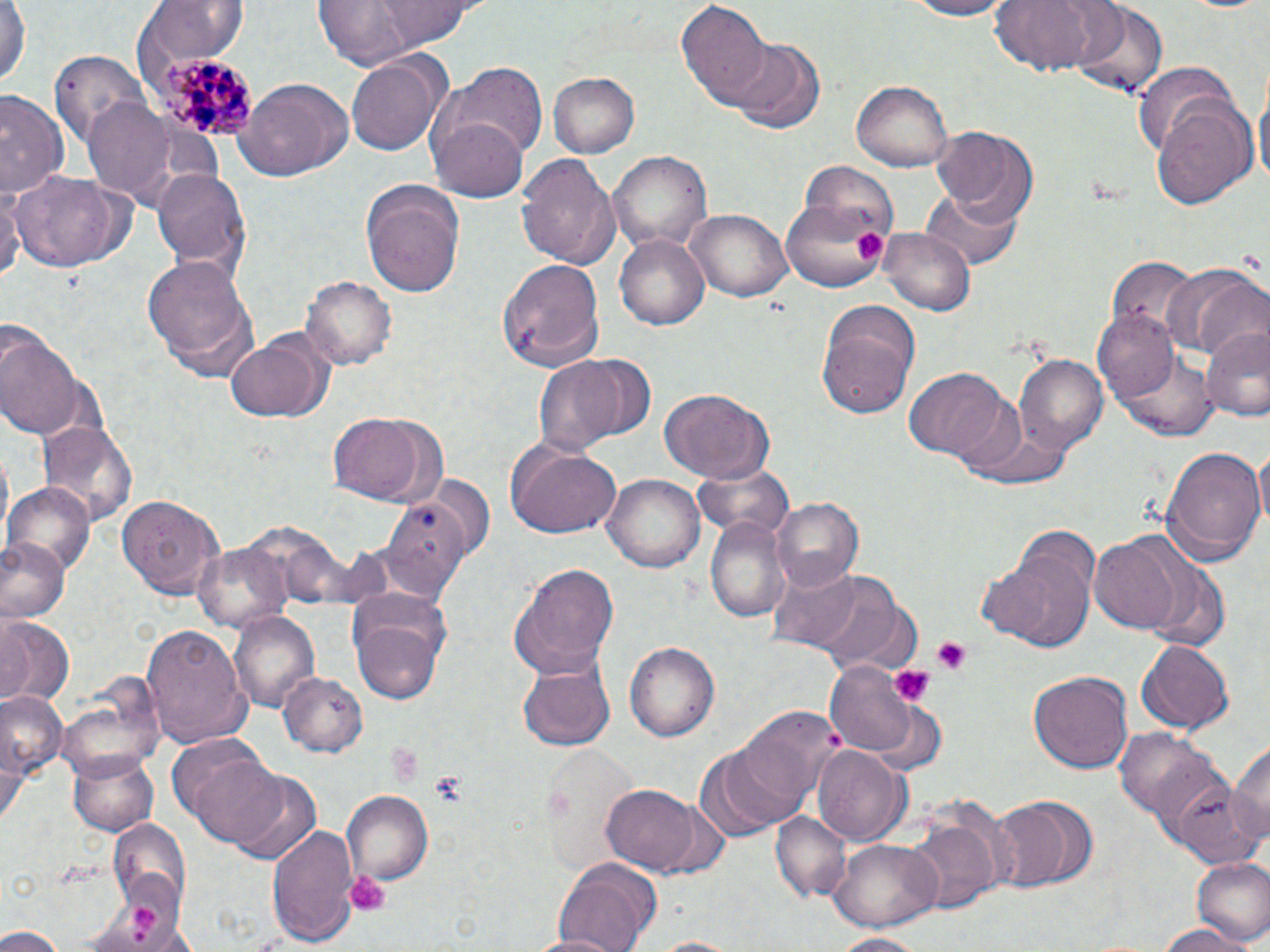

Summary:
  - Coordinate format: approximate bounding boxes as named x1/y1/x2/y2 corners in pixels
  - Uninfected red blood cell locations: (x1=1, y1=0, x2=30, y2=92), (x1=375, y1=0, x2=480, y2=47), (x1=898, y1=0, x2=1021, y2=20), (x1=994, y1=0, x2=1108, y2=77), (x1=142, y1=2, x2=248, y2=72), (x1=310, y1=2, x2=457, y2=67), (x1=677, y1=2, x2=770, y2=109), (x1=1070, y1=2, x2=1169, y2=101), (x1=728, y1=36, x2=829, y2=135), (x1=345, y1=50, x2=448, y2=157), (x1=49, y1=51, x2=153, y2=157), (x1=1133, y1=64, x2=1236, y2=154), (x1=451, y1=65, x2=549, y2=158), (x1=549, y1=73, x2=641, y2=158), (x1=236, y1=79, x2=353, y2=184), (x1=429, y1=81, x2=537, y2=203), (x1=852, y1=81, x2=953, y2=172), (x1=1255, y1=81, x2=1270, y2=193), (x1=0, y1=92, x2=64, y2=202), (x1=1147, y1=95, x2=1256, y2=208), (x1=83, y1=99, x2=178, y2=205), (x1=931, y1=125, x2=1039, y2=226), (x1=608, y1=152, x2=712, y2=255), (x1=516, y1=153, x2=620, y2=270), (x1=149, y1=166, x2=251, y2=276), (x1=9, y1=169, x2=134, y2=274), (x1=0, y1=176, x2=21, y2=289), (x1=359, y1=177, x2=466, y2=297), (x1=923, y1=185, x2=1022, y2=271), (x1=782, y1=188, x2=892, y2=294), (x1=682, y1=209, x2=793, y2=304), (x1=881, y1=228, x2=973, y2=315), (x1=613, y1=232, x2=710, y2=332), (x1=142, y1=249, x2=262, y2=380), (x1=1105, y1=257, x2=1197, y2=340), (x1=499, y1=258, x2=606, y2=370), (x1=1164, y1=265, x2=1263, y2=357), (x1=302, y1=274, x2=398, y2=372), (x1=814, y1=296, x2=922, y2=417), (x1=1093, y1=310, x2=1183, y2=406), (x1=1200, y1=324, x2=1270, y2=422), (x1=226, y1=328, x2=333, y2=423), (x1=0, y1=330, x2=84, y2=443), (x1=1116, y1=347, x2=1216, y2=440), (x1=564, y1=352, x2=657, y2=442), (x1=1013, y1=354, x2=1108, y2=454), (x1=531, y1=356, x2=628, y2=457), (x1=906, y1=369, x2=1012, y2=461), (x1=659, y1=389, x2=773, y2=482), (x1=964, y1=413, x2=1079, y2=489), (x1=327, y1=414, x2=434, y2=504), (x1=36, y1=418, x2=138, y2=526), (x1=505, y1=442, x2=621, y2=538), (x1=1254, y1=444, x2=1270, y2=536), (x1=1163, y1=445, x2=1266, y2=564), (x1=692, y1=461, x2=796, y2=541), (x1=606, y1=471, x2=705, y2=571), (x1=428, y1=473, x2=493, y2=555), (x1=6, y1=485, x2=94, y2=578), (x1=118, y1=494, x2=226, y2=597), (x1=374, y1=497, x2=470, y2=605), (x1=768, y1=498, x2=864, y2=589), (x1=705, y1=515, x2=791, y2=625), (x1=0, y1=537, x2=68, y2=625), (x1=1089, y1=537, x2=1183, y2=634), (x1=194, y1=542, x2=293, y2=631), (x1=984, y1=542, x2=1099, y2=655), (x1=1141, y1=560, x2=1230, y2=652), (x1=509, y1=564, x2=621, y2=680), (x1=767, y1=565, x2=864, y2=651), (x1=804, y1=572, x2=922, y2=676), (x1=348, y1=593, x2=452, y2=703), (x1=2, y1=614, x2=74, y2=702), (x1=230, y1=614, x2=320, y2=714), (x1=139, y1=619, x2=252, y2=747), (x1=1135, y1=638, x2=1234, y2=735), (x1=624, y1=640, x2=720, y2=741), (x1=519, y1=661, x2=613, y2=751), (x1=822, y1=662, x2=937, y2=762), (x1=1027, y1=670, x2=1133, y2=775), (x1=278, y1=672, x2=365, y2=757), (x1=59, y1=678, x2=165, y2=777), (x1=1, y1=688, x2=65, y2=790), (x1=738, y1=706, x2=842, y2=810), (x1=1115, y1=727, x2=1227, y2=828), (x1=1229, y1=732, x2=1270, y2=847), (x1=697, y1=741, x2=809, y2=840), (x1=545, y1=748, x2=640, y2=873), (x1=812, y1=748, x2=911, y2=845), (x1=70, y1=750, x2=158, y2=836), (x1=187, y1=752, x2=291, y2=845), (x1=228, y1=771, x2=323, y2=867), (x1=601, y1=783, x2=709, y2=876), (x1=1174, y1=785, x2=1264, y2=868), (x1=341, y1=790, x2=433, y2=887), (x1=987, y1=794, x2=1098, y2=894), (x1=773, y1=813, x2=850, y2=901), (x1=907, y1=816, x2=1003, y2=912), (x1=110, y1=817, x2=190, y2=911), (x1=267, y1=822, x2=360, y2=951), (x1=827, y1=837, x2=942, y2=933), (x1=1191, y1=856, x2=1270, y2=946), (x1=551, y1=858, x2=663, y2=951), (x1=1155, y1=921, x2=1253, y2=952), (x1=0, y1=925, x2=65, y2=952), (x1=522, y1=931, x2=630, y2=952), (x1=826, y1=932, x2=936, y2=951), (x1=640, y1=935, x2=751, y2=951)
  - Platelet locations: (x1=852, y1=228, x2=888, y2=266), (x1=928, y1=637, x2=970, y2=675), (x1=890, y1=664, x2=935, y2=707), (x1=384, y1=744, x2=425, y2=785), (x1=431, y1=773, x2=466, y2=805), (x1=347, y1=870, x2=389, y2=914), (x1=128, y1=904, x2=158, y2=935)
  - Plasmodium malariae-infected red blood cell locations: (x1=147, y1=54, x2=260, y2=143)
  - Slide-level diagnosis: Plasmodium malariae
  - Image size: 1270×952 pixels
  - Preparation: thin blood film
  - Stain: May-Grünwald-Giemsa
  - Modality: optical microscopy
  - Field of view: single
  - Magnification: 1000x